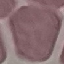
Summary:
  - Result: no malaria parasites seen
  - Preparation: thin blood smear
  - Capture: smartphone through the microscope eyepiece
  - Stain: Giemsa
  - Image type: cell patch, automatically extracted from a larger field of view and resized to 64 × 64 pixels